Assess the morphology of the erythrocytes.
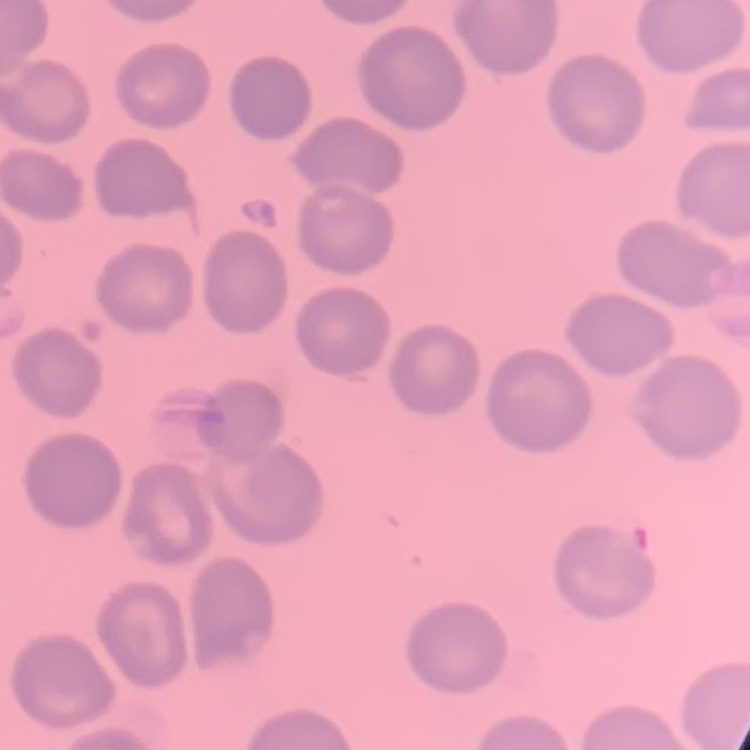

They show no rouleaux formation.

image type = square crop of a larger photomicrograph
stain = Field's or Giemsa
preparation = thin blood film